Assess the morphology of the erythrocytes.
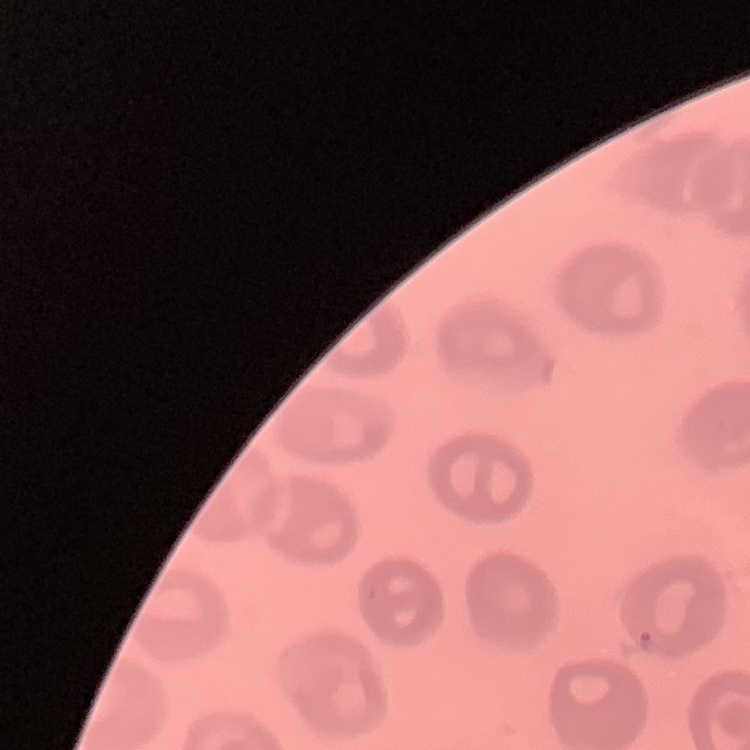
No rouleaux formation.

Summary:
  - Preparation: thin blood smear
  - Image type: one tile cut from a larger photomicrograph
  - Stain: Field's or Giemsa